Name the parasite shown.
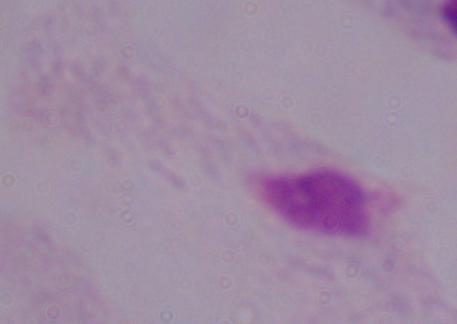
This is a trichomonad.

{
  "magnification": "1000x",
  "modality": "photomicrograph"
}